Outline each blood parasite and name the species.
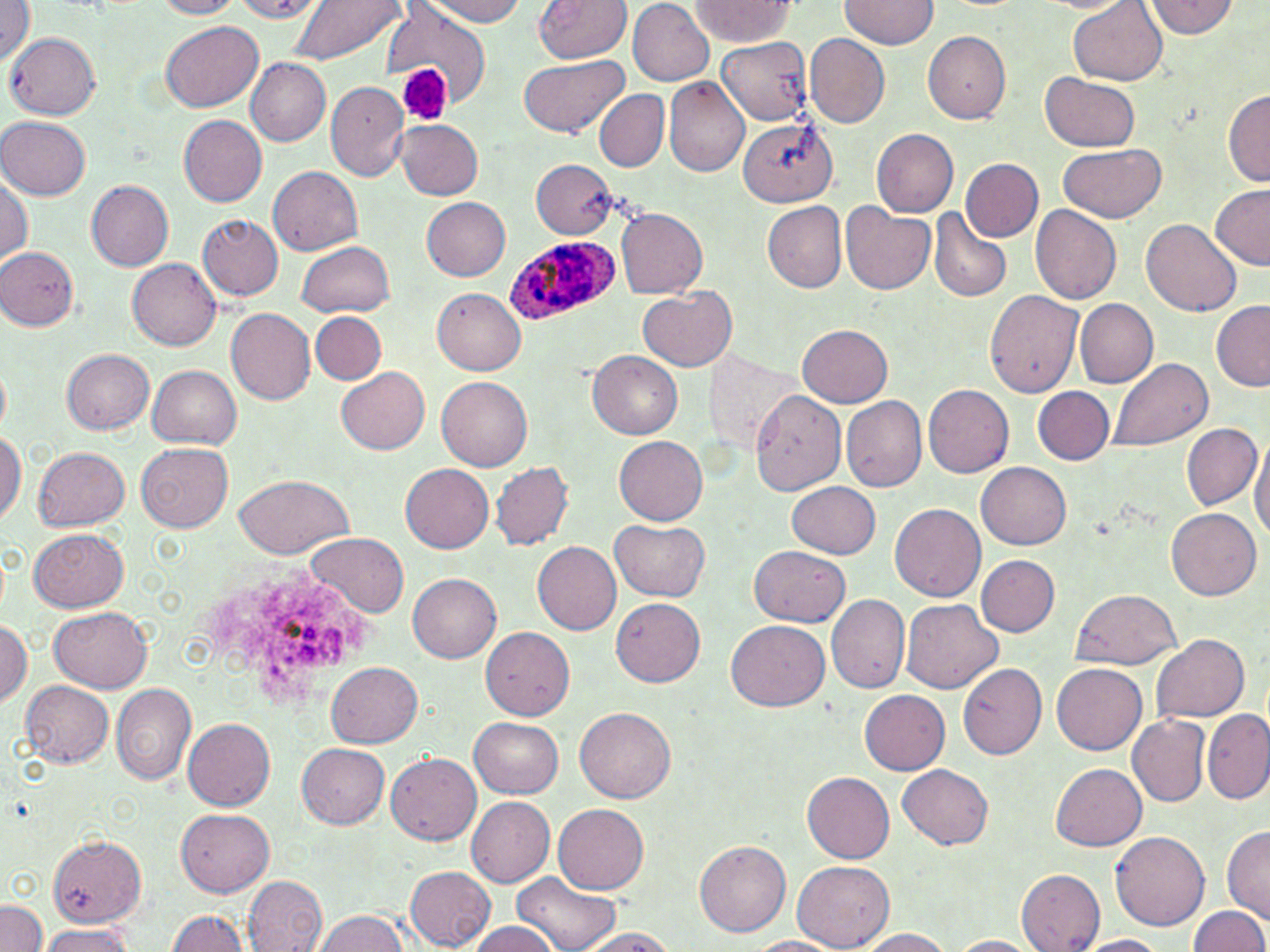
Approximate bounding boxes as (x1, y1, x2, y2) in pixels.
Plasmodium ovale-infected red blood cells: (503, 234, 615, 325).
No Plasmodium falciparum, Plasmodium malariae, Plasmodium vivax, Babesia divergens, or Trypanosoma brucei observed.

slide-level diagnosis = Plasmodium ovale
image size = 1270×952 pixels
stain = May-Grünwald-Giemsa
magnification = 1000x
platelet locations = approximate bounding boxes as (x1, y1, x2, y2) in pixels: (399, 63, 452, 125)
modality = light microscopy
preparation = thin blood smear
uninfected red blood cell locations = approximate bounding boxes as (x1, y1, x2, y2) in pixels: (1, 0, 35, 68), (152, 0, 245, 19), (230, 0, 326, 22), (287, 0, 404, 64), (419, 0, 529, 25), (534, 0, 632, 64), (627, 0, 715, 86), (841, 0, 938, 51), (1069, 0, 1169, 86), (1146, 0, 1238, 39), (689, 1, 796, 47), (383, 5, 491, 100), (159, 22, 265, 113), (923, 30, 1011, 123), (7, 33, 99, 120), (805, 33, 890, 130), (716, 37, 815, 125), (518, 54, 630, 139), (246, 59, 331, 146), (1042, 70, 1140, 150), (664, 78, 751, 178), (326, 81, 412, 181), (1222, 88, 1270, 186), (594, 90, 668, 170), (178, 114, 267, 206), (1, 116, 90, 199), (738, 117, 834, 210), (396, 119, 483, 199), (870, 126, 959, 217), (1058, 145, 1166, 222), (962, 158, 1043, 242), (531, 159, 618, 237), (267, 164, 363, 255), (1, 174, 33, 262), (86, 179, 174, 270), (1209, 184, 1269, 270), (422, 198, 510, 280), (762, 201, 847, 293), (1031, 204, 1122, 304), (840, 205, 935, 294), (615, 208, 709, 299), (928, 208, 1012, 304), (198, 214, 283, 300), (1142, 217, 1242, 316), (297, 240, 395, 316), (1, 247, 80, 330), (126, 258, 222, 351), (433, 288, 527, 373), (638, 288, 737, 372), (986, 289, 1084, 398), (1074, 299, 1158, 389), (1211, 299, 1270, 390), (226, 308, 318, 404), (311, 310, 387, 385), (798, 323, 894, 406), (61, 348, 154, 434), (588, 351, 682, 439), (708, 352, 795, 451), (1109, 358, 1214, 452), (0, 359, 11, 437), (148, 365, 241, 448), (336, 366, 431, 455), (438, 376, 531, 469), (924, 385, 1014, 478), (1032, 386, 1115, 464), (749, 389, 845, 496), (841, 395, 927, 492), (1182, 424, 1261, 509), (0, 430, 23, 527), (1249, 434, 1270, 541), (615, 436, 709, 524), (137, 442, 233, 531), (34, 446, 131, 530), (490, 461, 574, 550), (976, 461, 1071, 549), (401, 463, 495, 551), (235, 473, 351, 560), (787, 480, 881, 558), (891, 502, 986, 601), (1166, 506, 1260, 600), (611, 520, 710, 601), (28, 527, 130, 612), (306, 534, 410, 618), (532, 541, 622, 635), (748, 545, 851, 626), (977, 555, 1060, 636), (408, 571, 501, 662), (1070, 589, 1181, 670), (825, 593, 910, 693), (612, 598, 704, 686), (901, 598, 1002, 693), (49, 605, 154, 691), (727, 619, 829, 711), (0, 620, 32, 705), (481, 626, 575, 719), (1152, 633, 1250, 722), (329, 662, 423, 748), (959, 662, 1046, 759), (1052, 663, 1147, 754), (20, 680, 114, 768), (111, 683, 197, 785), (860, 691, 949, 773), (575, 706, 675, 802), (1202, 710, 1269, 802), (1127, 713, 1211, 806), (469, 717, 563, 798), (183, 718, 275, 812), (298, 743, 389, 829), (388, 753, 481, 845), (1051, 762, 1148, 849), (898, 763, 994, 849), (803, 772, 895, 863), (467, 797, 555, 887), (553, 803, 648, 894), (176, 808, 275, 897), (1222, 826, 1270, 925), (1112, 832, 1210, 932), (48, 838, 149, 928), (693, 841, 791, 937), (793, 862, 894, 950), (406, 867, 496, 951), (1016, 869, 1106, 951), (513, 871, 620, 952), (244, 875, 329, 952), (0, 900, 47, 952), (1186, 905, 1269, 952), (167, 910, 249, 952), (312, 910, 411, 952), (468, 921, 562, 952), (36, 925, 136, 952), (575, 928, 680, 952), (856, 928, 955, 952), (744, 936, 844, 952), (949, 936, 1040, 952), (1072, 936, 1171, 952)
field of view = one of a larger specimen